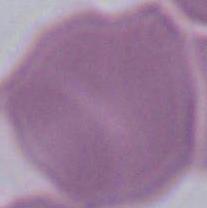
modality = micrograph
identification = erythrocyte
magnification = 1000x